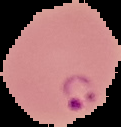

Malaria status: parasitized. Image is 121×127 pixels. From a thin blood film. The area outside the segmented cell region is set to black.